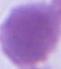

Summary:
  - Modality: photomicrograph
  - Magnification: 1000x
  - Identification: erythrocyte